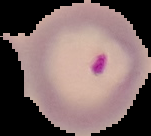

image type = segmented cell region on a black background
image size = 151×136 pixels
preparation = thin blood smear
malaria status = parasitized